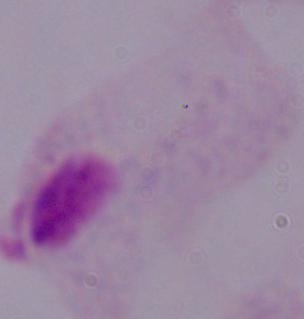

Summary:
  - Modality: photomicrograph
  - Identification: trichomonad
  - Magnification: 1000x